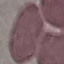
result = no malaria parasites seen
stain = Giemsa
image type = automatically extracted cell patch, resized to 64 × 64 pixels
preparation = thin smear
capture = smartphone camera at the microscope eyepiece